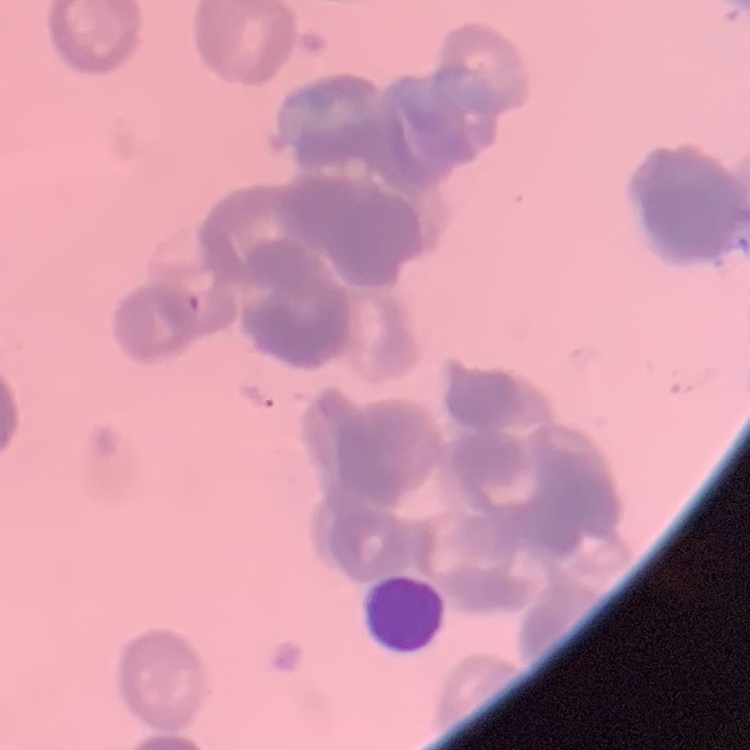 The erythrocytes show rouleaux formation. Field's or Giemsa stain. Thin blood smear. Square crop of a larger photomicrograph.